Name the cell type shown.
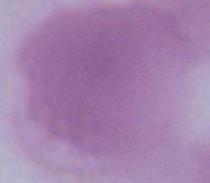
An erythrocyte.

modality = photomicrograph
magnification = 1000x